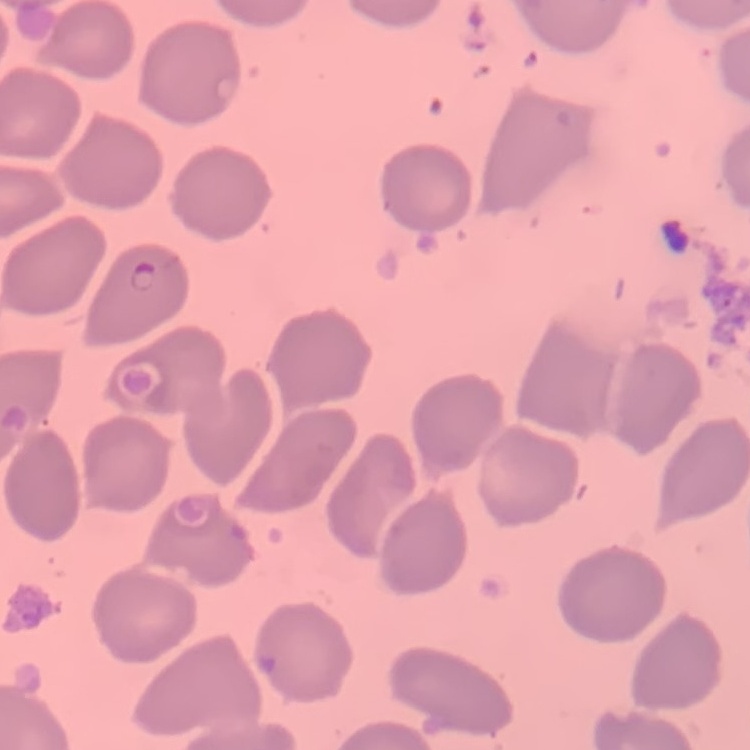

Summary:
  - Red blood cell morphology: no rouleaux formation
  - Stain: Field's or Giemsa
  - Image type: one tile cut from a larger photomicrograph
  - Preparation: thin blood smear